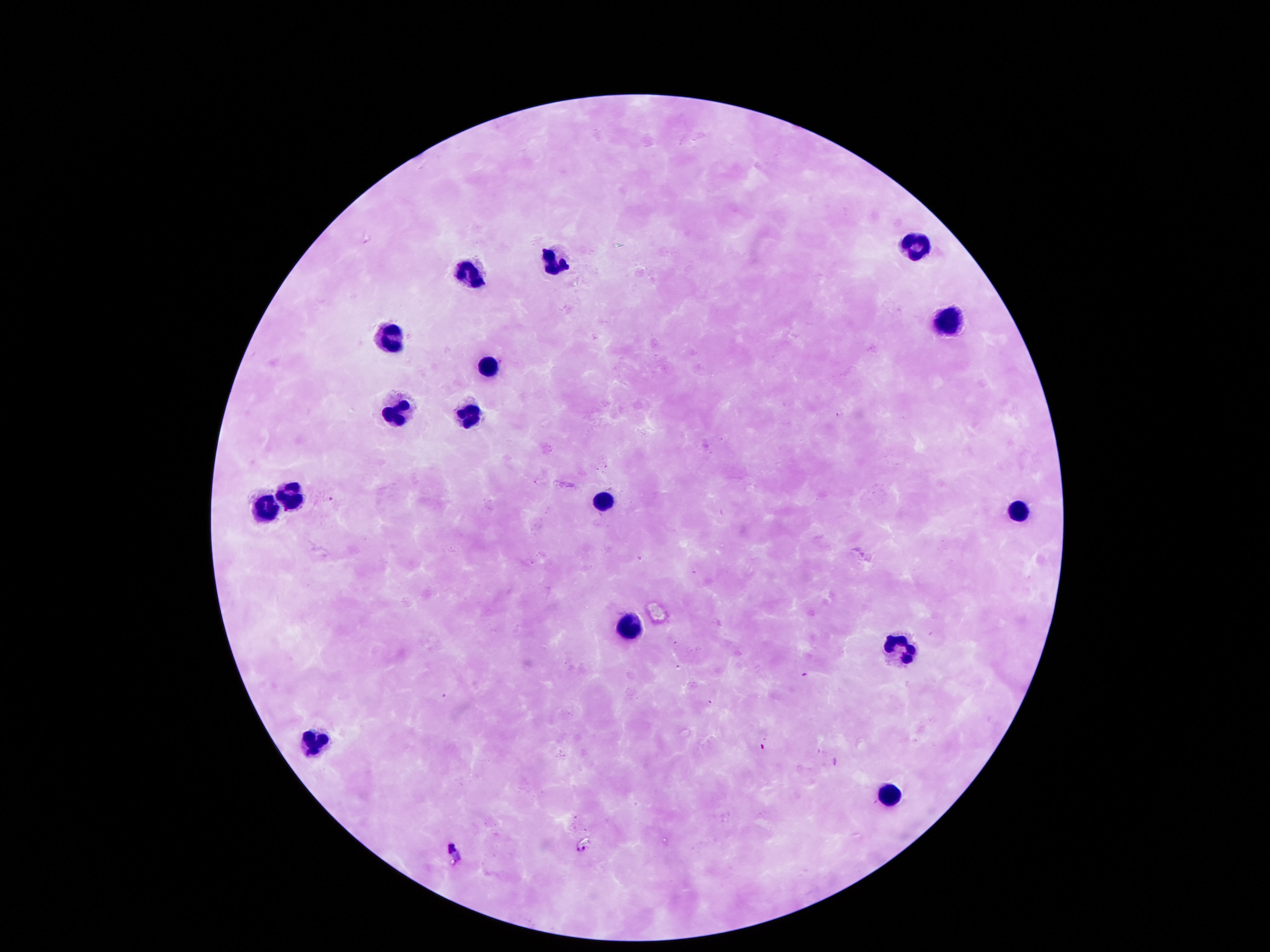

Approximate object centers, in pixels from the top-left corner.
Summary:
  - Leukocyte locations: (x=918, y=244), (x=555, y=258), (x=467, y=274), (x=951, y=327), (x=390, y=335), (x=487, y=362), (x=393, y=401), (x=464, y=412), (x=289, y=496), (x=595, y=499), (x=259, y=506), (x=1019, y=513), (x=629, y=623), (x=898, y=650), (x=313, y=738), (x=891, y=792)
  - Magnification: 100x
  - Stain: Giemsa
  - Field of view: single
  - Patient malaria status: negative
  - Preparation: thick peripheral-blood smear
  - Image size: 1270×952 pixels
  - Capture: smartphone camera through the microscope eyepiece